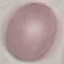
Malaria status: uninfected. Giemsa-stained preparation. Cell patch, automatically extracted from a larger field of view and resized to 64 × 64 pixels. Thin blood smear. Photographed with a smartphone camera at the microscope eyepiece.